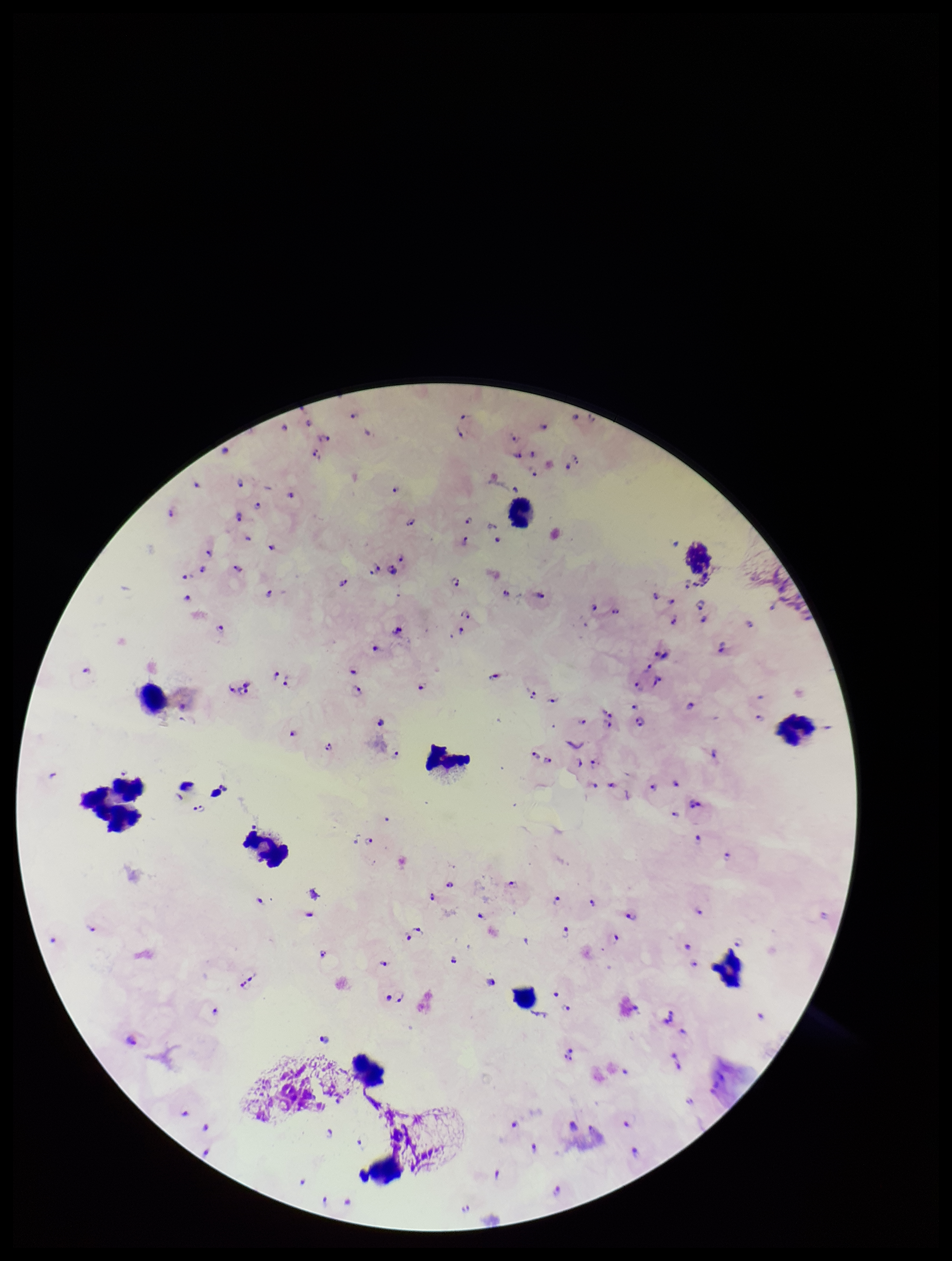
{
  "capture": "smartphone photograph through the microscope eyepiece",
  "patient_malaria_status": "infected",
  "stain": "Giemsa",
  "plasmodium_parasites": "identified",
  "parasite_count": 100,
  "preparation": "thick smear",
  "species_reported_for_this_patient": "Plasmodium falciparum",
  "field_of_view": "one from this slide",
  "leukocyte_count": 12,
  "image_size": "952×1261 pixels"
}